Classify this cell by malaria status.
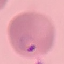

It is parasitized.

Acquired by smartphone through the microscope eyepiece. Giemsa-stained preparation. Thin smear of blood. Automatically extracted cell patch, resized to 64 × 64 pixels.